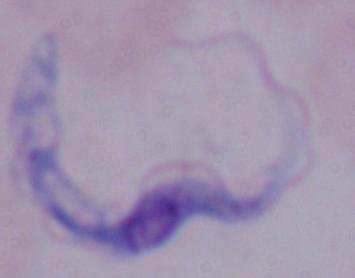
magnification: 1000x
identification: trypanosome
modality: micrograph